Assess this cell for malaria.
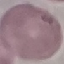

Uninfected.

Photographed with a smartphone camera at the microscope eyepiece. Thin blood smear. Giemsa stain. Automatically extracted cell patch, resized to 64 × 64 pixels.